Assess this cell for malaria.
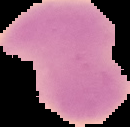
Uninfected.

Summary:
  - Image size: 130×127 pixels
  - Preparation: thin blood smear
  - Image type: cell region segmented out of the field of view; surrounding area masked to black